Report the malaria status of this cell.
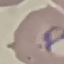

It is parasitized.

Summary:
  - Image type: cell patch, automatically extracted from a larger field of view and resized to 64 × 64 pixels
  - Capture: smartphone camera at the microscope eyepiece
  - Stain: Giemsa
  - Preparation: thin blood smear